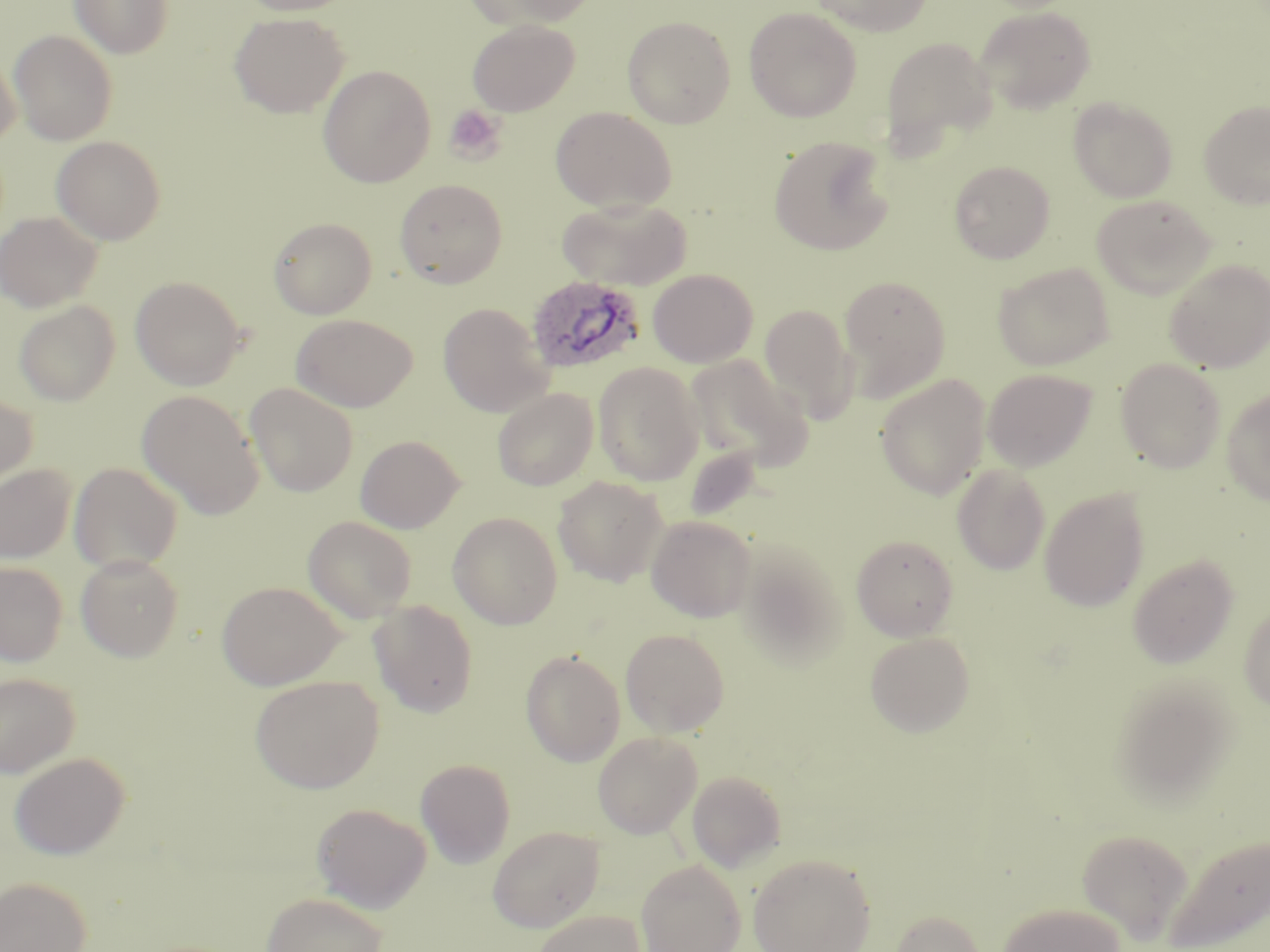

slide-level diagnosis = Plasmodium ovale
modality = light microscopy
Plasmodium ovale-infected red blood cell locations = approximate bounding boxes as named x1/y1/x2/y2 corners in pixels: (x1=525, y1=275, x2=647, y2=375)
image size = 1270×952 pixels
uninfected red blood cell locations = approximate bounding boxes as named x1/y1/x2/y2 corners in pixels: (x1=70, y1=0, x2=173, y2=59), (x1=236, y1=0, x2=357, y2=16), (x1=465, y1=0, x2=596, y2=30), (x1=809, y1=0, x2=933, y2=36), (x1=743, y1=6, x2=862, y2=122), (x1=975, y1=6, x2=1096, y2=114), (x1=229, y1=12, x2=348, y2=118), (x1=622, y1=15, x2=736, y2=128), (x1=467, y1=19, x2=579, y2=116), (x1=9, y1=30, x2=118, y2=145), (x1=880, y1=36, x2=997, y2=154), (x1=0, y1=47, x2=21, y2=147), (x1=318, y1=65, x2=436, y2=187), (x1=1068, y1=97, x2=1177, y2=202), (x1=1198, y1=100, x2=1270, y2=209), (x1=551, y1=107, x2=676, y2=213), (x1=51, y1=135, x2=166, y2=245), (x1=768, y1=135, x2=894, y2=256), (x1=949, y1=160, x2=1055, y2=264), (x1=394, y1=179, x2=507, y2=288), (x1=1091, y1=194, x2=1216, y2=298), (x1=556, y1=197, x2=692, y2=290), (x1=0, y1=211, x2=102, y2=313), (x1=268, y1=217, x2=377, y2=319), (x1=1165, y1=259, x2=1270, y2=372), (x1=992, y1=262, x2=1114, y2=371), (x1=648, y1=268, x2=758, y2=368), (x1=130, y1=275, x2=246, y2=390), (x1=839, y1=275, x2=951, y2=400), (x1=13, y1=300, x2=120, y2=406), (x1=438, y1=303, x2=552, y2=416), (x1=759, y1=303, x2=857, y2=421), (x1=291, y1=314, x2=416, y2=412), (x1=685, y1=355, x2=811, y2=471), (x1=1116, y1=358, x2=1226, y2=473), (x1=593, y1=362, x2=704, y2=486), (x1=983, y1=368, x2=1097, y2=472), (x1=875, y1=374, x2=991, y2=500), (x1=245, y1=383, x2=358, y2=497), (x1=1221, y1=387, x2=1270, y2=506), (x1=492, y1=388, x2=598, y2=491), (x1=136, y1=390, x2=264, y2=519), (x1=0, y1=391, x2=38, y2=492), (x1=355, y1=434, x2=464, y2=533), (x1=69, y1=462, x2=183, y2=574), (x1=0, y1=464, x2=76, y2=563), (x1=952, y1=464, x2=1050, y2=574), (x1=553, y1=476, x2=668, y2=587), (x1=1039, y1=487, x2=1150, y2=612), (x1=447, y1=511, x2=563, y2=629), (x1=645, y1=514, x2=757, y2=621), (x1=302, y1=515, x2=418, y2=623), (x1=851, y1=534, x2=958, y2=641), (x1=733, y1=540, x2=849, y2=668), (x1=75, y1=553, x2=184, y2=662), (x1=1127, y1=553, x2=1239, y2=669), (x1=0, y1=561, x2=68, y2=666), (x1=216, y1=581, x2=345, y2=690), (x1=368, y1=600, x2=478, y2=717), (x1=1239, y1=602, x2=1270, y2=713), (x1=620, y1=628, x2=730, y2=737), (x1=864, y1=632, x2=975, y2=736), (x1=520, y1=649, x2=626, y2=767), (x1=0, y1=672, x2=80, y2=777), (x1=250, y1=674, x2=384, y2=793), (x1=1111, y1=675, x2=1240, y2=803), (x1=593, y1=731, x2=701, y2=838), (x1=9, y1=752, x2=130, y2=859), (x1=415, y1=758, x2=516, y2=868), (x1=687, y1=770, x2=786, y2=872), (x1=311, y1=802, x2=432, y2=913), (x1=487, y1=825, x2=605, y2=932), (x1=1077, y1=829, x2=1193, y2=941), (x1=1163, y1=832, x2=1270, y2=952), (x1=747, y1=852, x2=877, y2=952), (x1=636, y1=859, x2=745, y2=952), (x1=0, y1=876, x2=91, y2=952), (x1=261, y1=891, x2=389, y2=952), (x1=997, y1=901, x2=1126, y2=952), (x1=530, y1=909, x2=647, y2=952), (x1=890, y1=909, x2=986, y2=952)
preparation = thin blood smear
magnification = 1000x
stain = May-Grünwald-Giemsa
platelet locations = approximate bounding boxes as named x1/y1/x2/y2 corners in pixels: (x1=444, y1=104, x2=507, y2=164)
field of view = single